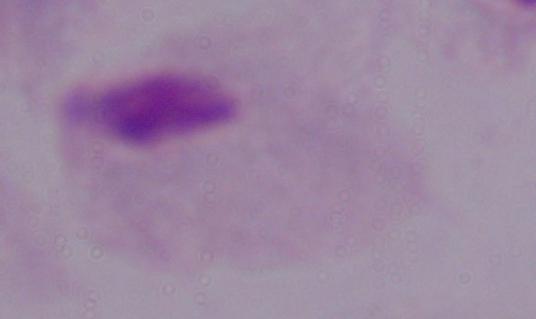
Summary:
  - Magnification: 1000x
  - Identification: trichomonad
  - Modality: micrograph